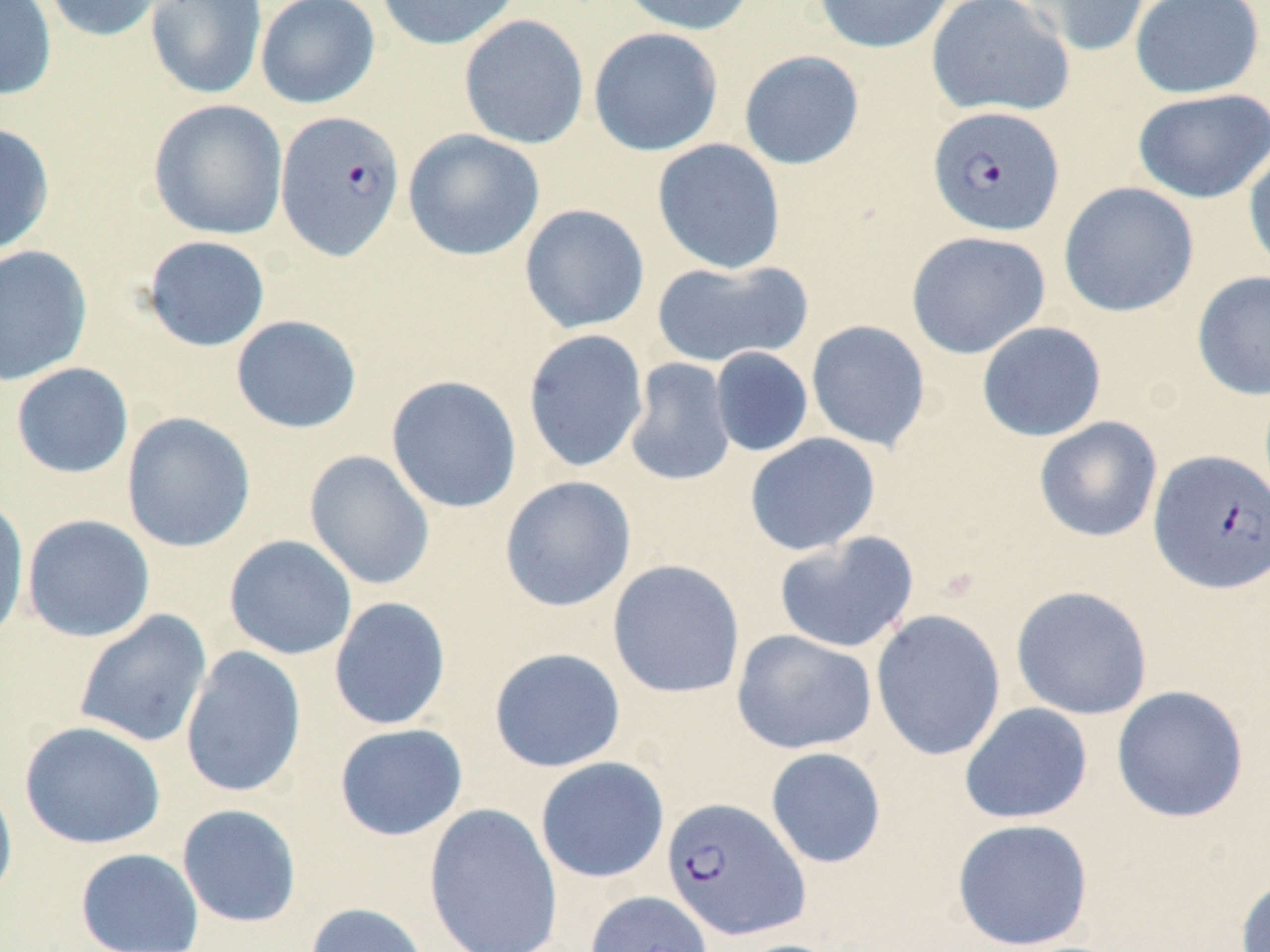
slide-level diagnosis = Plasmodium falciparum
magnification = 1000x
uninfected red blood cell locations = approximate bounding boxes as named x1/y1/x2/y2 corners in pixels: (x1=0, y1=0, x2=57, y2=102), (x1=40, y1=0, x2=165, y2=42), (x1=145, y1=0, x2=268, y2=100), (x1=255, y1=0, x2=380, y2=109), (x1=376, y1=0, x2=522, y2=50), (x1=617, y1=0, x2=757, y2=36), (x1=811, y1=0, x2=956, y2=54), (x1=925, y1=0, x2=1075, y2=118), (x1=1017, y1=0, x2=1152, y2=58), (x1=1129, y1=0, x2=1265, y2=100), (x1=458, y1=14, x2=589, y2=150), (x1=588, y1=27, x2=724, y2=157), (x1=738, y1=50, x2=865, y2=170), (x1=1132, y1=88, x2=1270, y2=204), (x1=148, y1=99, x2=288, y2=240), (x1=0, y1=122, x2=55, y2=257), (x1=402, y1=129, x2=545, y2=261), (x1=652, y1=138, x2=786, y2=275), (x1=1243, y1=142, x2=1270, y2=280), (x1=1058, y1=181, x2=1199, y2=318), (x1=518, y1=203, x2=650, y2=334), (x1=906, y1=230, x2=1051, y2=359), (x1=142, y1=235, x2=271, y2=352), (x1=0, y1=244, x2=93, y2=387), (x1=651, y1=258, x2=813, y2=369), (x1=1191, y1=270, x2=1270, y2=400), (x1=230, y1=315, x2=362, y2=434), (x1=806, y1=319, x2=931, y2=452), (x1=976, y1=321, x2=1107, y2=442), (x1=522, y1=328, x2=649, y2=474), (x1=709, y1=346, x2=814, y2=458), (x1=624, y1=357, x2=736, y2=487), (x1=10, y1=362, x2=134, y2=479), (x1=385, y1=375, x2=522, y2=514), (x1=121, y1=412, x2=256, y2=552), (x1=1033, y1=416, x2=1163, y2=543), (x1=744, y1=432, x2=881, y2=556), (x1=304, y1=450, x2=436, y2=591), (x1=499, y1=475, x2=637, y2=612), (x1=0, y1=496, x2=30, y2=645), (x1=21, y1=514, x2=156, y2=642), (x1=773, y1=531, x2=919, y2=654), (x1=223, y1=535, x2=357, y2=660), (x1=607, y1=560, x2=746, y2=699), (x1=1010, y1=586, x2=1153, y2=720), (x1=329, y1=596, x2=452, y2=731), (x1=870, y1=609, x2=1007, y2=762), (x1=73, y1=610, x2=213, y2=749), (x1=731, y1=629, x2=877, y2=755), (x1=180, y1=646, x2=306, y2=799), (x1=489, y1=647, x2=626, y2=773), (x1=1111, y1=685, x2=1249, y2=823), (x1=959, y1=702, x2=1093, y2=824), (x1=18, y1=721, x2=166, y2=850), (x1=334, y1=723, x2=468, y2=841), (x1=765, y1=747, x2=887, y2=869), (x1=535, y1=757, x2=670, y2=883), (x1=0, y1=772, x2=19, y2=908), (x1=423, y1=802, x2=563, y2=952), (x1=176, y1=803, x2=302, y2=928), (x1=951, y1=817, x2=1093, y2=952), (x1=75, y1=847, x2=204, y2=952), (x1=1235, y1=874, x2=1270, y2=952), (x1=585, y1=890, x2=712, y2=952), (x1=304, y1=902, x2=431, y2=952), (x1=726, y1=939, x2=850, y2=952)
stain = May-Grünwald-Giemsa
Plasmodium falciparum-infected red blood cell locations = approximate bounding boxes as named x1/y1/x2/y2 corners in pixels: (x1=927, y1=105, x2=1065, y2=237), (x1=275, y1=111, x2=406, y2=261), (x1=1148, y1=450, x2=1270, y2=594), (x1=661, y1=796, x2=810, y2=941)
preparation = thin blood smear
image size = 1270×952 pixels
field of view = one of a larger specimen
modality = light microscopy